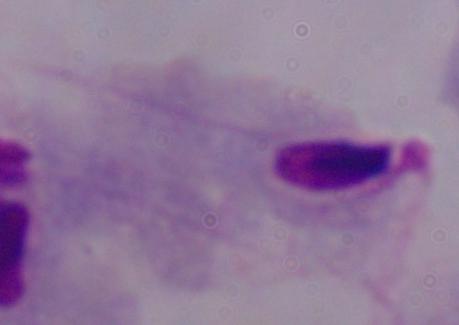

modality = photomicrograph
identification = trichomonad
magnification = 1000x